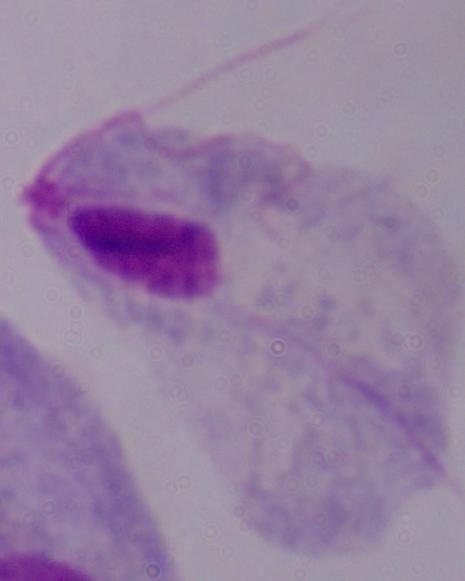
magnification = 1000x
identification = trichomonad
modality = micrograph